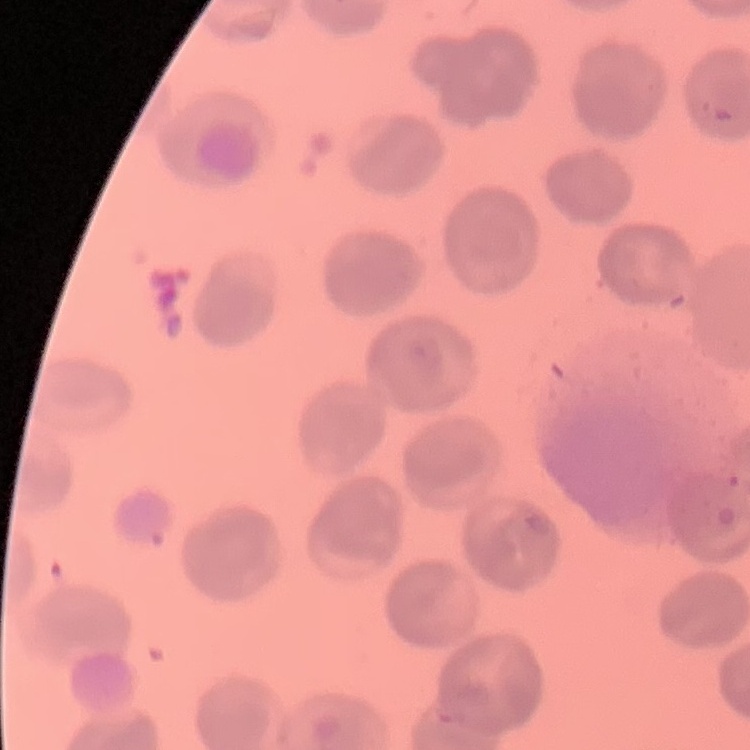

Summary:
  - Erythrocyte morphology: no rouleaux formation
  - Preparation: thin blood film
  - Stain: Field's or Giemsa
  - Image type: square crop of a larger photomicrograph